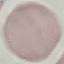
Result: negative for malaria parasites. Photographed with a smartphone camera at the microscope eyepiece. Thin blood film. Automatically extracted cell patch, resized to 64 × 64 pixels. Giemsa-stained preparation.